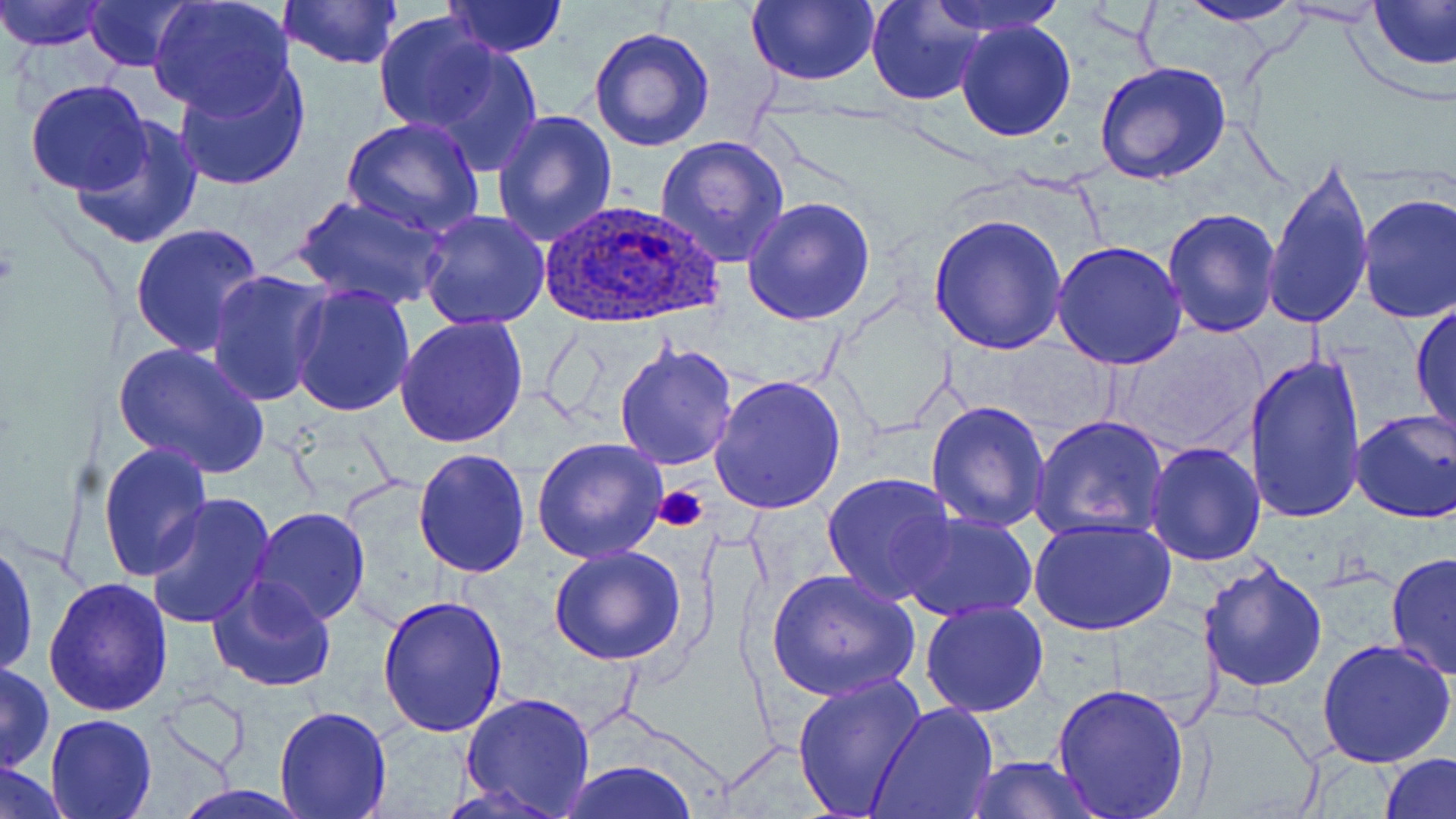
slide-level diagnosis = Plasmodium ovale
preparation = thin blood film
modality = light microscopy
platelet locations = approximate bounding boxes as (x1,y1)-(x2,y2) corner pairs in pixels: (655,486)-(708,533)
magnification = 1000x
uninfected red blood cell locations = approximate bounding boxes as (x1,y1)-(x2,y2) corner pairs in pixels: (0,0)-(110,52), (83,0)-(198,71), (146,0)-(295,118), (746,0)-(879,87), (868,0)-(986,106), (928,0)-(1067,37), (1171,0)-(1312,27), (1371,0)-(1455,70), (277,1)-(404,72), (443,1)-(567,57), (372,12)-(504,135), (954,19)-(1077,142), (587,26)-(715,153), (409,41)-(543,174), (173,59)-(314,193), (1094,61)-(1232,187), (24,79)-(152,195), (491,110)-(618,247), (341,116)-(485,240), (70,119)-(204,251), (654,136)-(790,266), (1261,150)-(1376,335), (1356,192)-(1456,322), (296,194)-(445,310), (742,195)-(876,324), (1162,207)-(1284,339), (419,209)-(551,331), (928,213)-(1069,355), (130,223)-(264,359), (1052,242)-(1186,371), (206,269)-(331,408), (289,285)-(415,416), (1410,299)-(1456,441), (394,313)-(532,450), (1112,326)-(1265,456), (613,340)-(739,470), (112,341)-(270,482), (1244,350)-(1367,528), (708,374)-(848,515), (926,401)-(1051,534), (1349,409)-(1456,523), (1031,413)-(1171,543), (532,437)-(667,562), (97,441)-(211,582), (1144,443)-(1264,566), (411,447)-(530,578), (822,471)-(958,605), (144,493)-(277,631), (248,508)-(371,627), (896,512)-(1038,620), (1028,517)-(1176,637), (0,539)-(38,680), (549,545)-(687,665), (1385,551)-(1456,680), (1196,559)-(1328,690), (766,568)-(920,702), (43,576)-(174,717), (208,576)-(339,693), (377,595)-(509,739), (920,600)-(1049,718), (1317,637)-(1456,769), (0,662)-(54,774), (792,672)-(928,819), (1051,682)-(1190,817), (459,692)-(597,816), (868,702)-(1000,819), (275,704)-(392,818), (45,713)-(157,818), (1378,751)-(1456,819), (968,755)-(1097,819), (2,759)-(70,818), (559,760)-(699,818), (169,785)-(314,819)
field of view = one of a larger specimen
image size = 1456×819 pixels
Plasmodium ovale-infected red blood cell locations = approximate bounding boxes as (x1,y1)-(x2,y2) corner pairs in pixels: (537,198)-(722,330)
stain = May-Grünwald-Giemsa